Describe the morphology of the red blood cells.
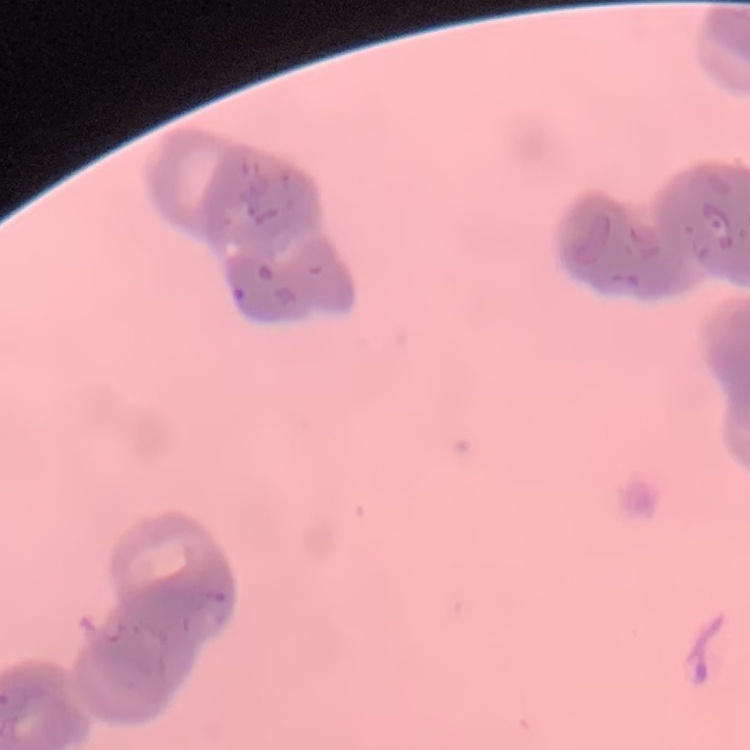
Rouleaux formation.

Square crop of a larger photomicrograph. Thin blood smear. Field's or Giemsa stain.